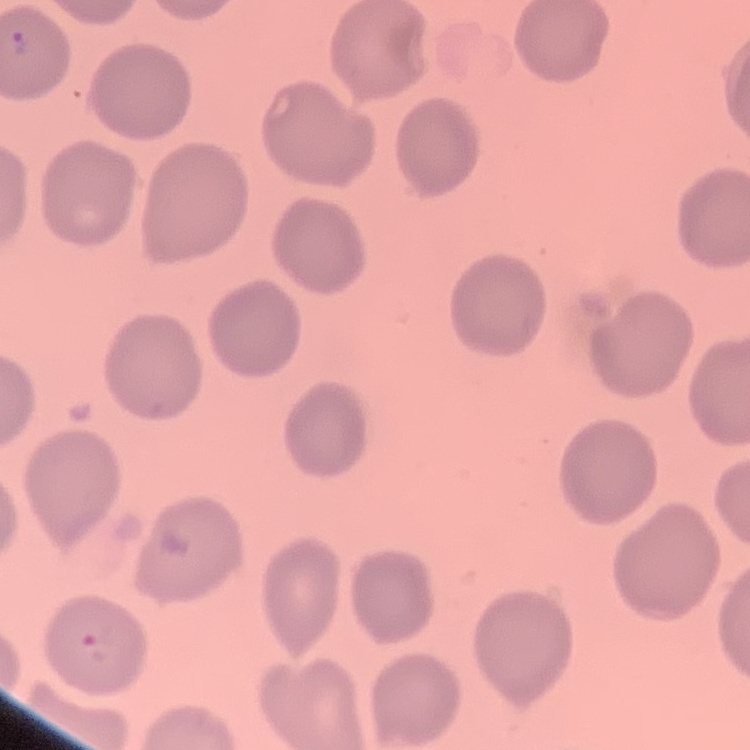

The erythrocytes exhibit no rouleaux formation. Thin peripheral smear. Field's or Giemsa stain. Square crop of a larger photomicrograph.